Assess the morphology of the red blood cells.
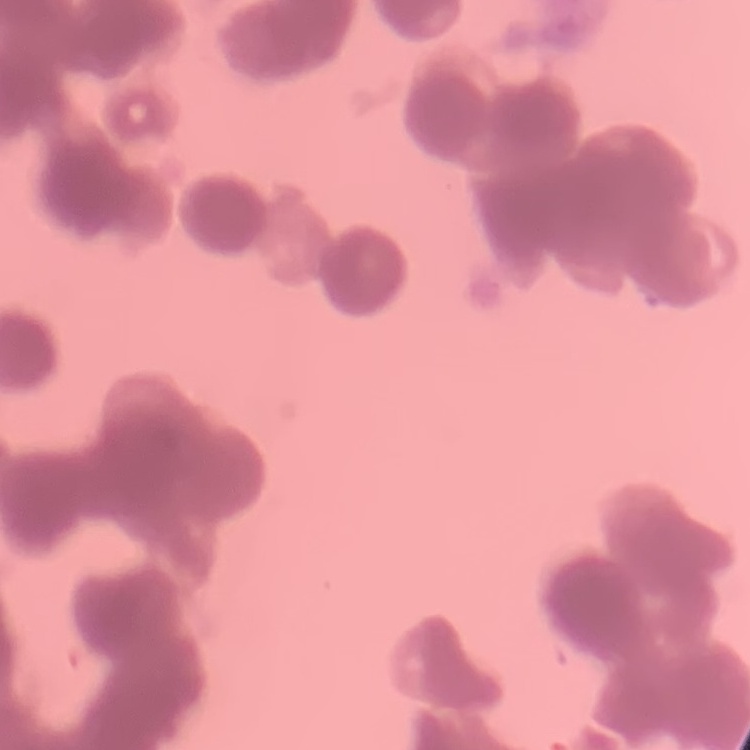

Rouleaux formation.

image type = square crop of a larger photomicrograph
preparation = thin peripheral smear
stain = Field's or Giemsa